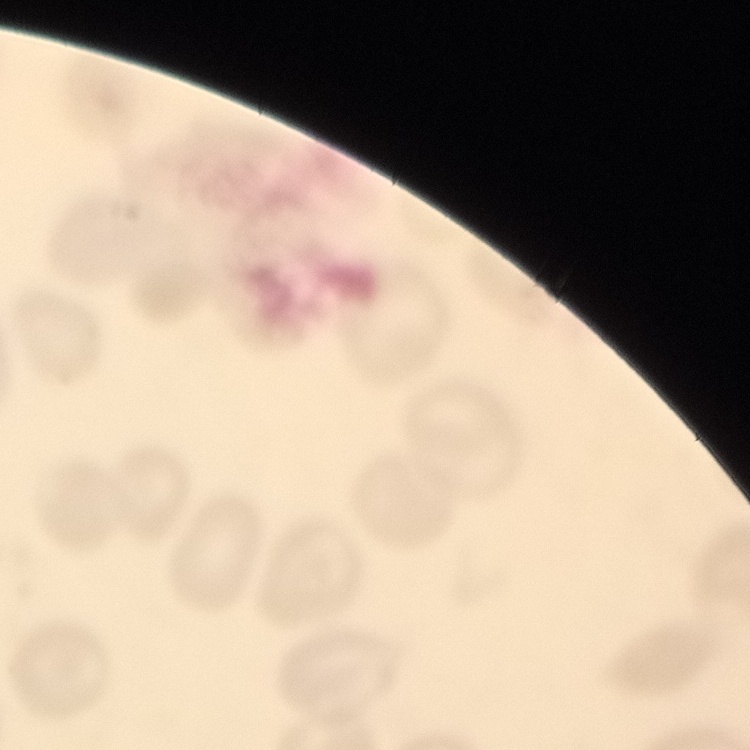
Summary:
  - Red blood cell morphology: no rouleaux formation
  - Preparation: thin blood smear
  - Image type: square crop of a larger photomicrograph
  - Stain: Field's or Giemsa